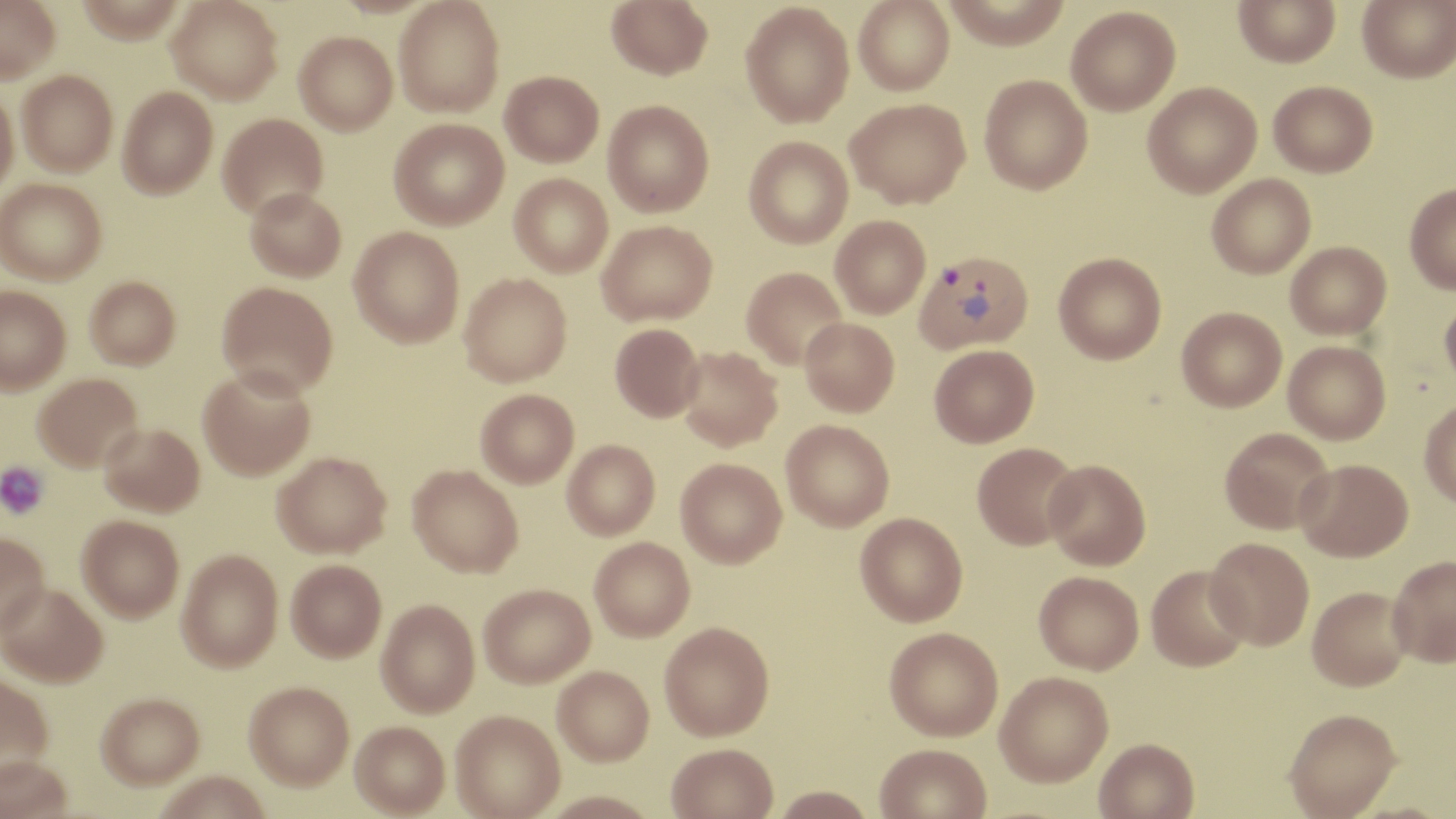
slide-level diagnosis = Plasmodium vivax
stain = May-Grünwald-Giemsa
magnification = 1000x
platelet locations = approximate bounding boxes as [x1, y1, x2, y2] in pixels: [0, 461, 49, 519]
field of view = single
preparation = thin blood smear
image size = 1456×819 pixels
Plasmodium vivax-infected red blood cell locations = approximate bounding boxes as [x1, y1, x2, y2] in pixels: [915, 250, 1034, 354]
modality = light microscopy
uninfected red blood cell locations = approximate bounding boxes as [x1, y1, x2, y2] in pixels: [0, 0, 60, 83], [75, 0, 186, 43], [167, 0, 283, 103], [393, 0, 505, 117], [606, 0, 713, 80], [853, 0, 955, 96], [942, 0, 1072, 50], [1233, 0, 1340, 67], [1357, 0, 1456, 83], [740, 2, 854, 127], [1066, 6, 1180, 116], [294, 32, 397, 135], [16, 70, 118, 176], [501, 70, 604, 167], [980, 74, 1092, 194], [1268, 81, 1377, 177], [1142, 82, 1262, 198], [118, 86, 218, 199], [0, 87, 19, 197], [845, 98, 970, 208], [603, 100, 714, 217], [218, 113, 328, 219], [389, 118, 509, 230], [744, 136, 853, 248], [509, 173, 613, 276], [1207, 174, 1316, 279], [1, 178, 106, 284], [1405, 184, 1456, 293], [245, 187, 346, 282], [830, 216, 930, 318], [596, 220, 717, 325], [349, 226, 465, 347], [1285, 241, 1391, 339], [1054, 252, 1166, 364], [741, 267, 847, 369], [459, 272, 572, 386], [85, 275, 180, 369], [217, 281, 338, 396], [0, 286, 71, 394], [1439, 294, 1456, 396], [1176, 307, 1287, 412], [800, 318, 899, 416], [610, 323, 704, 422], [1283, 340, 1391, 443], [929, 344, 1039, 446], [677, 346, 783, 450], [197, 367, 316, 481], [32, 372, 143, 471], [476, 388, 579, 488], [1419, 399, 1456, 508], [781, 419, 894, 531], [99, 422, 204, 516], [1220, 427, 1334, 534], [562, 439, 660, 539], [972, 442, 1081, 550], [273, 451, 391, 558], [676, 457, 787, 568], [1296, 458, 1413, 561], [1043, 459, 1151, 570], [408, 464, 523, 577], [855, 512, 968, 626], [77, 514, 184, 621], [0, 532, 49, 634], [590, 537, 696, 641], [1205, 537, 1314, 650], [176, 549, 283, 671], [1387, 555, 1456, 667], [286, 559, 386, 662], [1146, 565, 1251, 671], [1033, 571, 1143, 674], [0, 583, 108, 686], [479, 583, 595, 687], [1307, 586, 1413, 692], [376, 599, 480, 717], [659, 622, 774, 741], [883, 627, 1003, 742], [553, 666, 654, 766], [995, 672, 1113, 789], [0, 673, 54, 777], [244, 681, 354, 790], [96, 692, 205, 788], [1283, 709, 1401, 818], [450, 711, 565, 819], [350, 721, 450, 817], [1094, 740, 1199, 819], [875, 745, 992, 819], [667, 746, 778, 819], [0, 755, 73, 819], [155, 772, 271, 819], [771, 788, 876, 819], [541, 792, 660, 819]